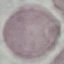
result: no malaria parasites seen
capture: smartphone camera at the microscope eyepiece
image_type: automatically extracted cell patch, resized to 64 × 64 pixels
preparation: thin smear
stain: Giemsa